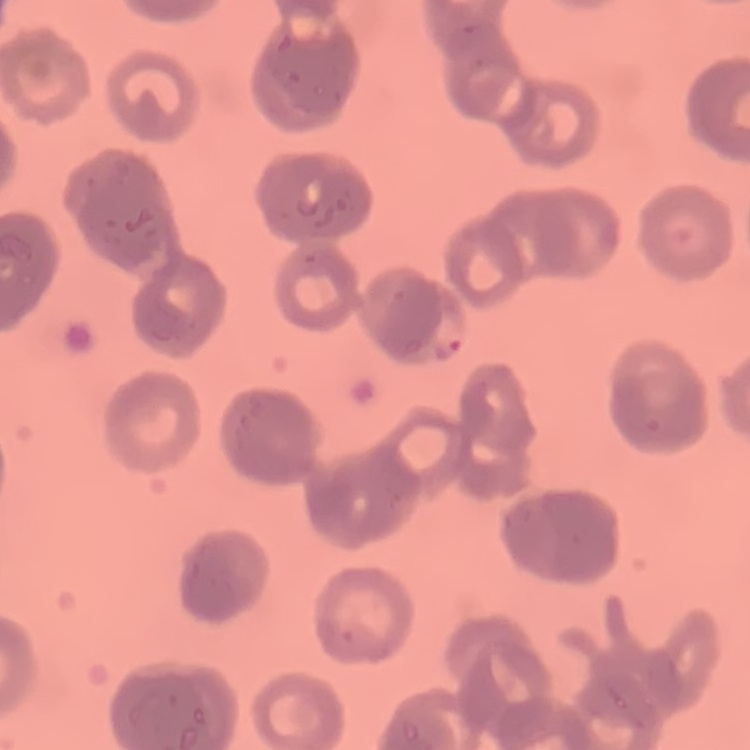
The erythrocytes show rouleaux formation. Thin peripheral smear. Square crop of a larger photomicrograph. Stained with either Field's or Giemsa.